Assess this cell for malaria.
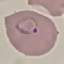

Parasitized.

Giemsa stain. Acquired by smartphone through the microscope eyepiece. Automatically extracted cell patch, resized to 64 × 64 pixels. Thin blood film.